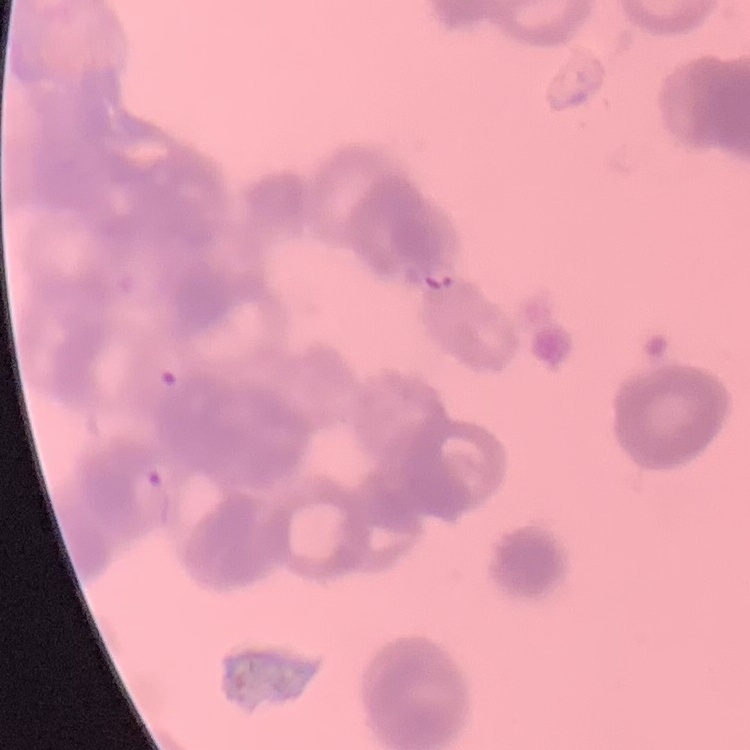
Summary:
  - Erythrocyte morphology: rouleaux formation
  - Stain: Field's or Giemsa
  - Image type: square crop of a larger photomicrograph
  - Preparation: thin peripheral smear